Name the parasite shown.
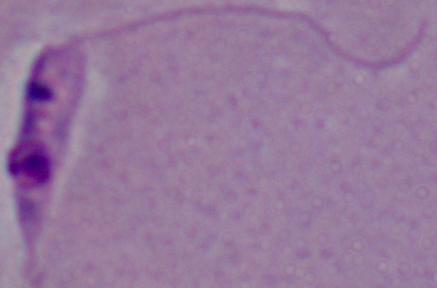
Leishmania.

Summary:
  - Magnification: 1000x
  - Modality: micrograph